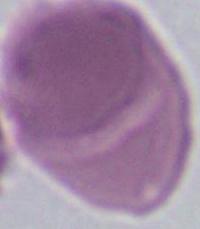 1000x magnification. Micrograph. An erythrocyte is seen.